Locate every Plasmodium parasite.
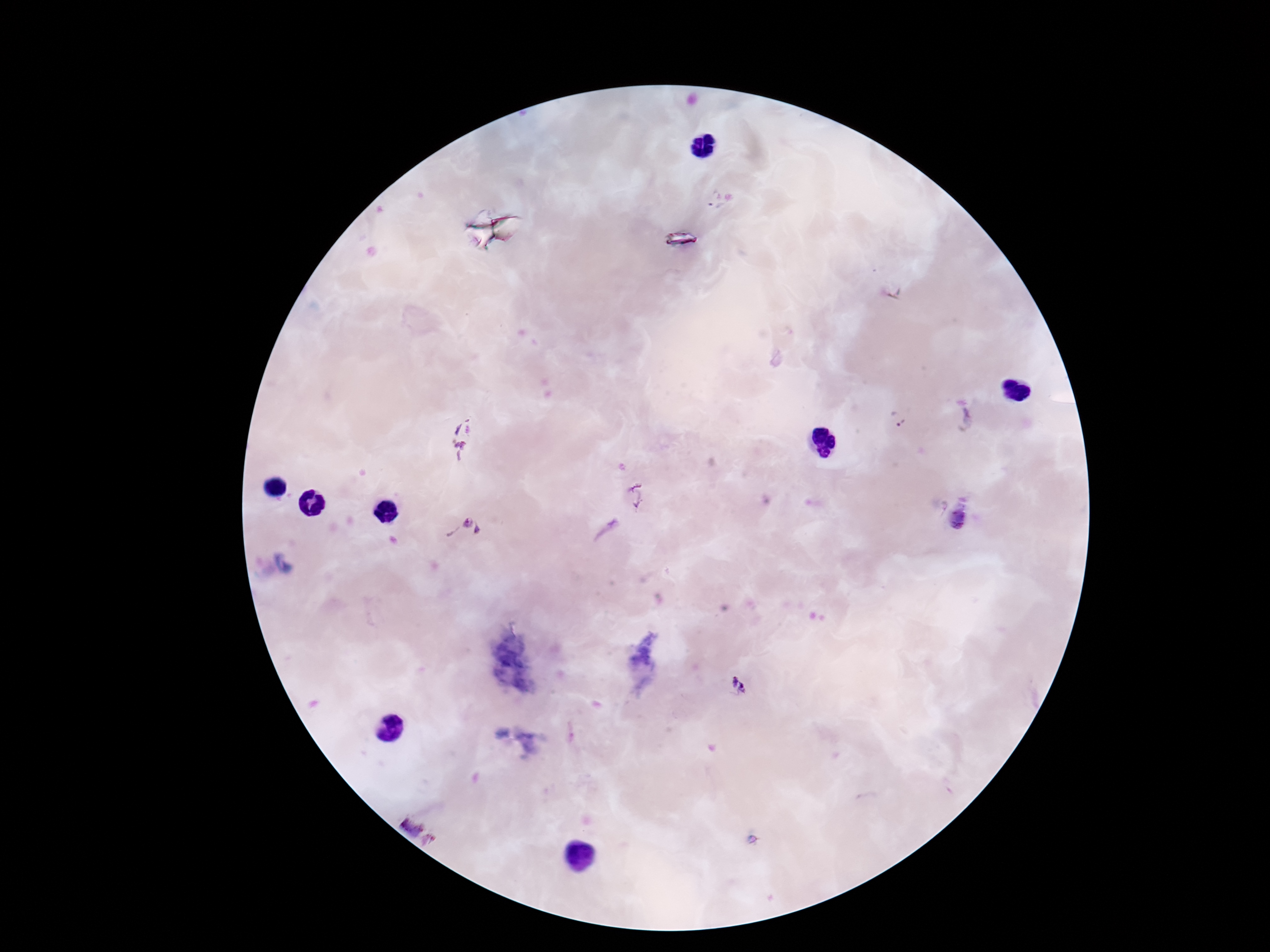

Approximate centers as {x, y} in pixels.
Plasmodium parasites: {711, 201}, {900, 418}, {963, 419}, {463, 438}, {637, 494}, {956, 519}, {464, 530}, {738, 685}, {406, 820}, {429, 841}.

Smartphone photograph taken through the microscope eyepiece. Image is 1270×952 pixels. 100x magnification. Patient malaria status: positive. One field from this slide. Giemsa stain. Thick blood smear.